Describe the morphology of the red blood cells.
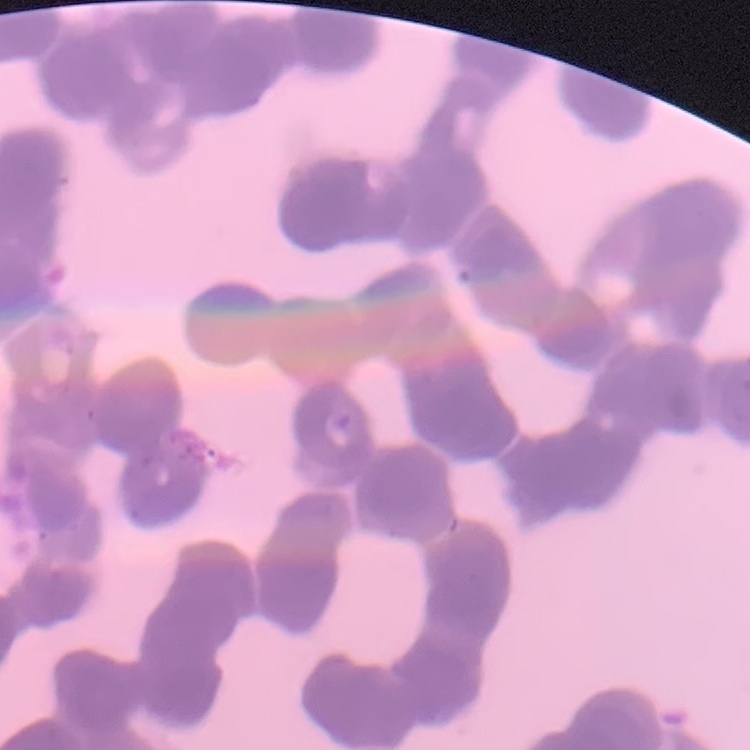
They show rouleaux formation.

Summary:
  - Stain: Field's or Giemsa
  - Preparation: thin blood film
  - Image type: square crop of a larger photomicrograph